Assess this cell for malaria.
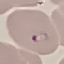

It is parasitized.

Summary:
  - Preparation: thin blood film
  - Capture: smartphone camera at the microscope eyepiece
  - Stain: Giemsa
  - Image type: cell patch, automatically extracted from a larger field of view and resized to 64 × 64 pixels